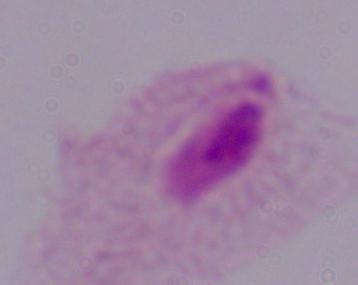
A trichomonad is shown. Micrograph. Captured at 1000x magnification.